Identify the cell.
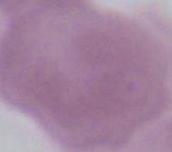
This is an erythrocyte.

{
  "modality": "photomicrograph",
  "magnification": "1000x"
}